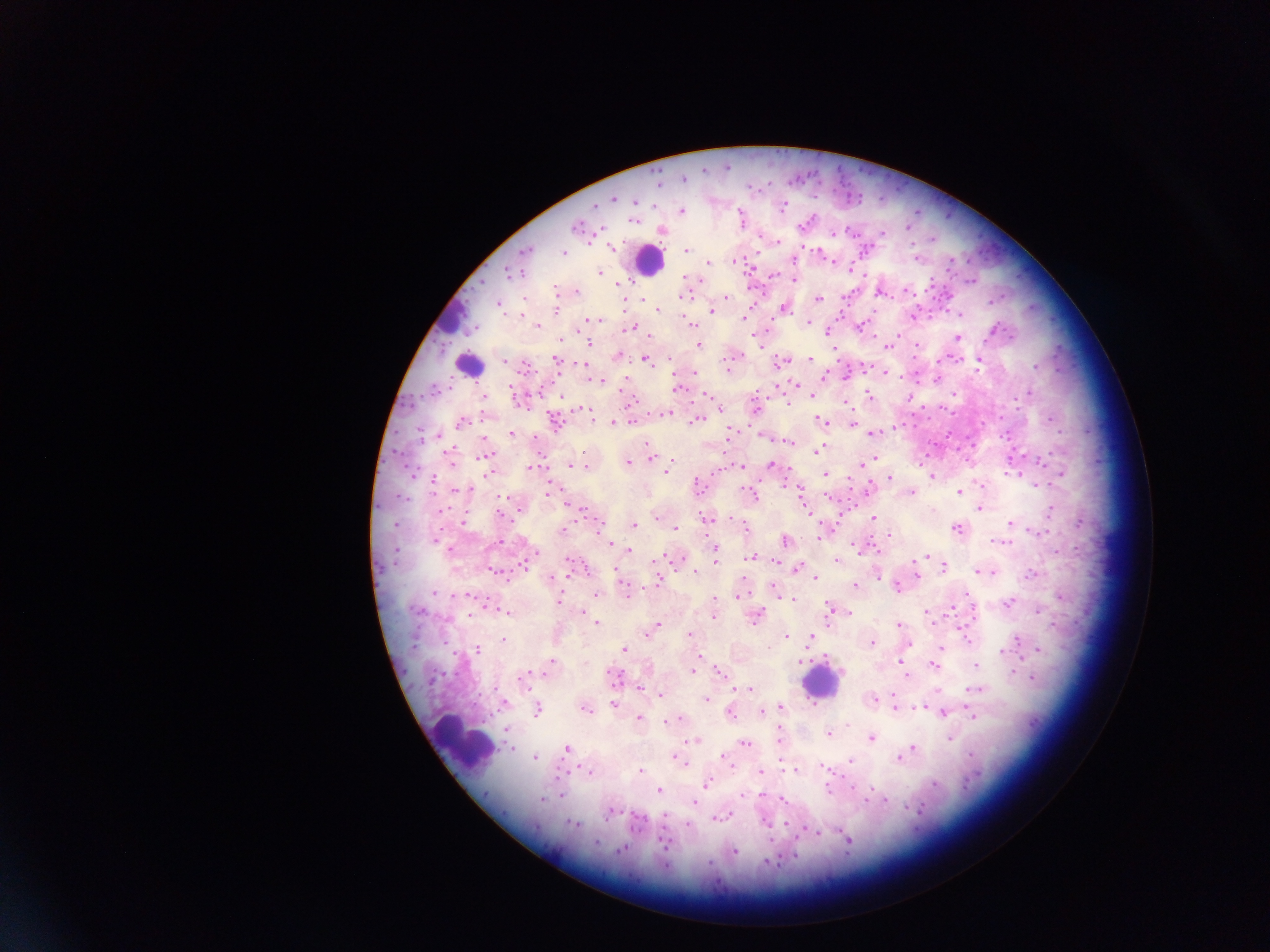

Approximate centers as [x, y] in pixels. Leukocyte locations: [647, 260], [444, 317], [470, 365], [821, 683], [463, 741]. Plasmodium parasite locations: [614, 201], [783, 207], [655, 208], [682, 212], [741, 219], [635, 223], [909, 228], [662, 233], [884, 235], [934, 240], [614, 249], [687, 251], [820, 254], [565, 255], [916, 259], [794, 260], [950, 261], [709, 264], [852, 272], [601, 274], [687, 278], [795, 279], [700, 282], [557, 291], [576, 292], [881, 294], [684, 297], [947, 297], [526, 299], [726, 299], [641, 300], [819, 301], [623, 302], [499, 304], [784, 310], [556, 311], [658, 312], [712, 313], [961, 316], [521, 317], [916, 317], [744, 319], [594, 320], [694, 326], [538, 328], [862, 328], [634, 330], [829, 332], [649, 335], [958, 337], [898, 338], [559, 339], [759, 340], [590, 344], [889, 345], [700, 346], [916, 346], [835, 349], [618, 356], [557, 359], [810, 360], [646, 361], [504, 362], [670, 362], [733, 362], [783, 363], [979, 363], [584, 365], [1037, 367], [730, 368], [694, 374], [884, 375], [826, 378], [601, 382], [796, 385], [677, 391], [1029, 394], [954, 395], [813, 396], [705, 397], [870, 397], [559, 399], [909, 399], [484, 400], [846, 401], [630, 403], [788, 405], [757, 407], [718, 409], [588, 414], [665, 415], [486, 416], [699, 420], [462, 423], [824, 423], [613, 424], [853, 426], [896, 429], [874, 434], [512, 435], [729, 435], [438, 438], [485, 440], [790, 443], [647, 444], [819, 451], [489, 457], [651, 458], [875, 459], [452, 462], [865, 462], [629, 463], [772, 465], [571, 466], [587, 467], [740, 468], [530, 469], [667, 470], [826, 474], [1016, 474], [1060, 476], [931, 477], [433, 480], [891, 480], [982, 485], [698, 487], [470, 491], [869, 491], [457, 493], [548, 493], [960, 493], [912, 494], [755, 498], [981, 510], [1050, 510], [808, 512], [656, 519], [875, 519], [708, 520], [465, 523], [1080, 523], [1011, 525], [745, 526], [598, 527], [635, 527], [564, 530], [676, 530], [958, 530], [828, 532], [1044, 533], [890, 536], [606, 540], [786, 541], [501, 542], [611, 544], [1004, 544], [859, 547], [871, 549], [450, 550], [631, 551], [716, 555], [661, 557], [752, 557], [926, 557], [838, 561], [527, 562], [655, 562], [615, 567], [580, 568], [798, 569], [944, 569], [916, 571], [977, 571], [696, 574], [992, 574], [1033, 575], [916, 576], [877, 577], [816, 578], [552, 579], [659, 584], [855, 586], [774, 590], [898, 590], [627, 592], [434, 593], [741, 593], [468, 596], [597, 596], [738, 597], [793, 598], [1060, 599], [968, 600], [558, 602], [1009, 604], [971, 608], [420, 613], [832, 613], [1038, 613], [508, 614], [582, 614], [927, 616], [471, 617], [713, 617], [758, 617], [598, 624], [900, 626], [655, 630], [965, 631], [690, 635], [788, 637], [812, 639], [1019, 640], [504, 641], [909, 644], [872, 645], [414, 648], [941, 648], [625, 651], [1038, 651], [479, 652], [1003, 652], [699, 656], [799, 662], [900, 663], [552, 664], [935, 666], [976, 666], [694, 671], [720, 673], [1014, 674], [615, 677], [907, 677], [1033, 679], [525, 684], [495, 687], [639, 688], [749, 690], [976, 690], [661, 695], [708, 701], [873, 701], [504, 705], [615, 706], [894, 706], [781, 708], [920, 710], [537, 712], [587, 712], [763, 712], [730, 713], [944, 713], [972, 716], [639, 718], [678, 720], [666, 722], [506, 730], [830, 735], [781, 736], [871, 739], [950, 739], [696, 743], [746, 745], [511, 750], [567, 750], [913, 751], [906, 755], [536, 758], [900, 759], [677, 760], [729, 762], [852, 762], [683, 764], [826, 769], [641, 771], [795, 772], [590, 773], [760, 773], [707, 785], [934, 785], [829, 789], [661, 791], [561, 797], [543, 800], [782, 800], [883, 802], [694, 804], [612, 814], [721, 817], [765, 823], [638, 824], [688, 824], [576, 826], [847, 843], [666, 844], [734, 854]. One field of view. Thick blood film. Image is 1270×952 pixels. Collected in Ghana. Mobile-phone photograph taken through the microscope.